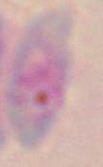
Summary:
  - Identification: Toxoplasma gondii
  - Magnification: 1000x
  - Modality: micrograph